Give the extent of all white blood cells.
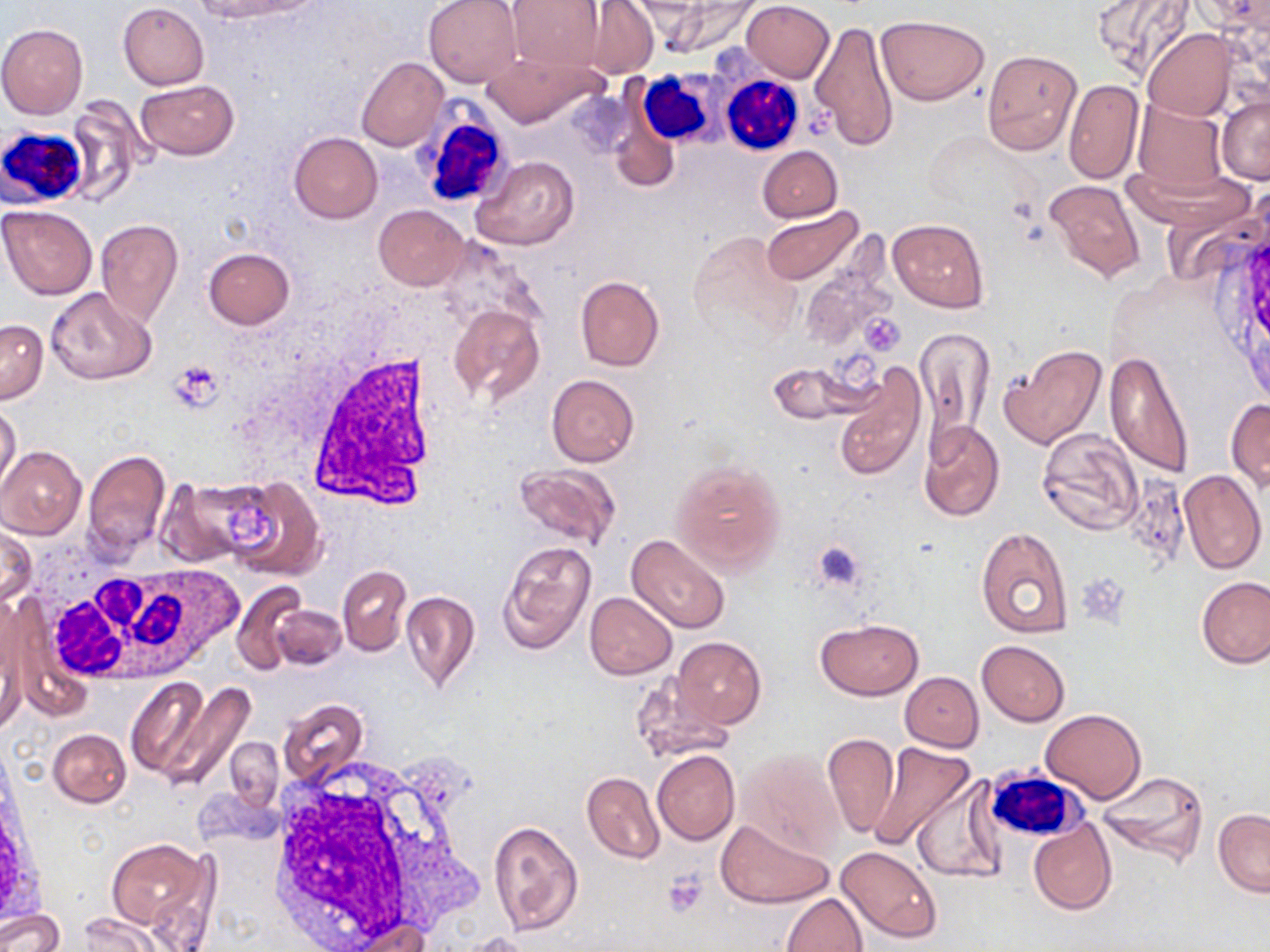

Approximate bounding boxes as [x1, y1, x2, y2] in pixels.
White blood cells: [641, 62, 733, 156], [720, 74, 805, 157], [415, 102, 517, 210], [0, 124, 93, 211], [308, 355, 440, 507], [32, 550, 242, 683], [264, 763, 478, 949], [984, 767, 1085, 845].

slide-level diagnosis = negative for blood parasites
uninfected red blood cell locations = approximate bounding boxes as [x1, y1, x2, y2] in pixels: [192, 0, 304, 22], [424, 0, 523, 87], [508, 0, 607, 72], [655, 0, 764, 57], [581, 1, 658, 79], [741, 1, 834, 82], [1092, 2, 1199, 83], [118, 3, 209, 89], [876, 15, 988, 105], [808, 18, 899, 151], [0, 23, 88, 118], [1142, 29, 1235, 121], [982, 49, 1082, 156], [480, 50, 605, 127], [356, 57, 448, 151], [135, 80, 238, 160], [1063, 80, 1144, 183], [1216, 94, 1269, 183], [64, 97, 149, 207], [1132, 101, 1227, 195], [610, 105, 681, 196], [289, 132, 382, 223], [757, 145, 842, 222], [474, 155, 579, 251], [1042, 177, 1144, 282], [373, 205, 468, 289], [0, 206, 97, 300], [762, 208, 862, 285], [888, 218, 988, 312], [95, 220, 184, 327], [688, 230, 802, 346], [801, 244, 899, 356], [203, 247, 295, 329], [574, 275, 665, 371], [46, 288, 157, 387], [447, 303, 545, 408], [0, 320, 47, 402], [917, 323, 992, 459], [999, 344, 1107, 450], [1103, 350, 1196, 478], [767, 363, 858, 424], [832, 365, 927, 480], [546, 374, 639, 467], [1227, 398, 1270, 493], [0, 401, 21, 494], [918, 420, 1004, 522], [1036, 428, 1144, 534], [1, 445, 86, 538], [83, 447, 171, 559], [672, 461, 786, 574], [510, 462, 619, 550], [1178, 469, 1267, 574], [224, 477, 325, 579], [160, 480, 259, 566], [0, 528, 38, 609], [975, 528, 1074, 637], [626, 535, 730, 634], [497, 539, 598, 653], [338, 564, 411, 655], [1197, 577, 1270, 669], [232, 581, 309, 674], [400, 589, 481, 693], [585, 592, 677, 679], [270, 604, 346, 671], [0, 612, 26, 731], [814, 619, 922, 700], [673, 636, 766, 729], [976, 640, 1070, 726], [632, 671, 735, 762], [900, 672, 983, 752], [124, 677, 210, 782], [161, 682, 254, 790], [277, 698, 368, 789], [1041, 708, 1145, 804], [47, 728, 131, 807], [822, 733, 899, 840], [225, 738, 283, 811], [867, 742, 975, 852], [652, 750, 740, 845], [736, 750, 844, 859], [1096, 770, 1209, 865], [582, 771, 665, 864], [911, 774, 1003, 885], [1213, 808, 1270, 898], [716, 819, 833, 909], [1029, 819, 1117, 915], [487, 820, 584, 935], [106, 840, 207, 930], [835, 846, 944, 944], [146, 890, 213, 952], [781, 892, 868, 952], [0, 909, 64, 952], [77, 914, 161, 951], [341, 917, 431, 951], [462, 931, 536, 952]
preparation = thin blood film
stain = May-Grünwald-Giemsa
magnification = 1000x
field of view = one of a larger specimen
platelet locations = approximate bounding boxes as [x1, y1, x2, y2] in pixels: [860, 315, 905, 356], [169, 361, 225, 412], [812, 540, 865, 593], [664, 872, 709, 917]
image size = 1270×952 pixels
modality = light microscopy